Give a bounding box for every parasitised red blood cell, every trophozoite, every gametocyte, every leukocyte, and every artifact (platelet-like body, stain precipitate, or debris).
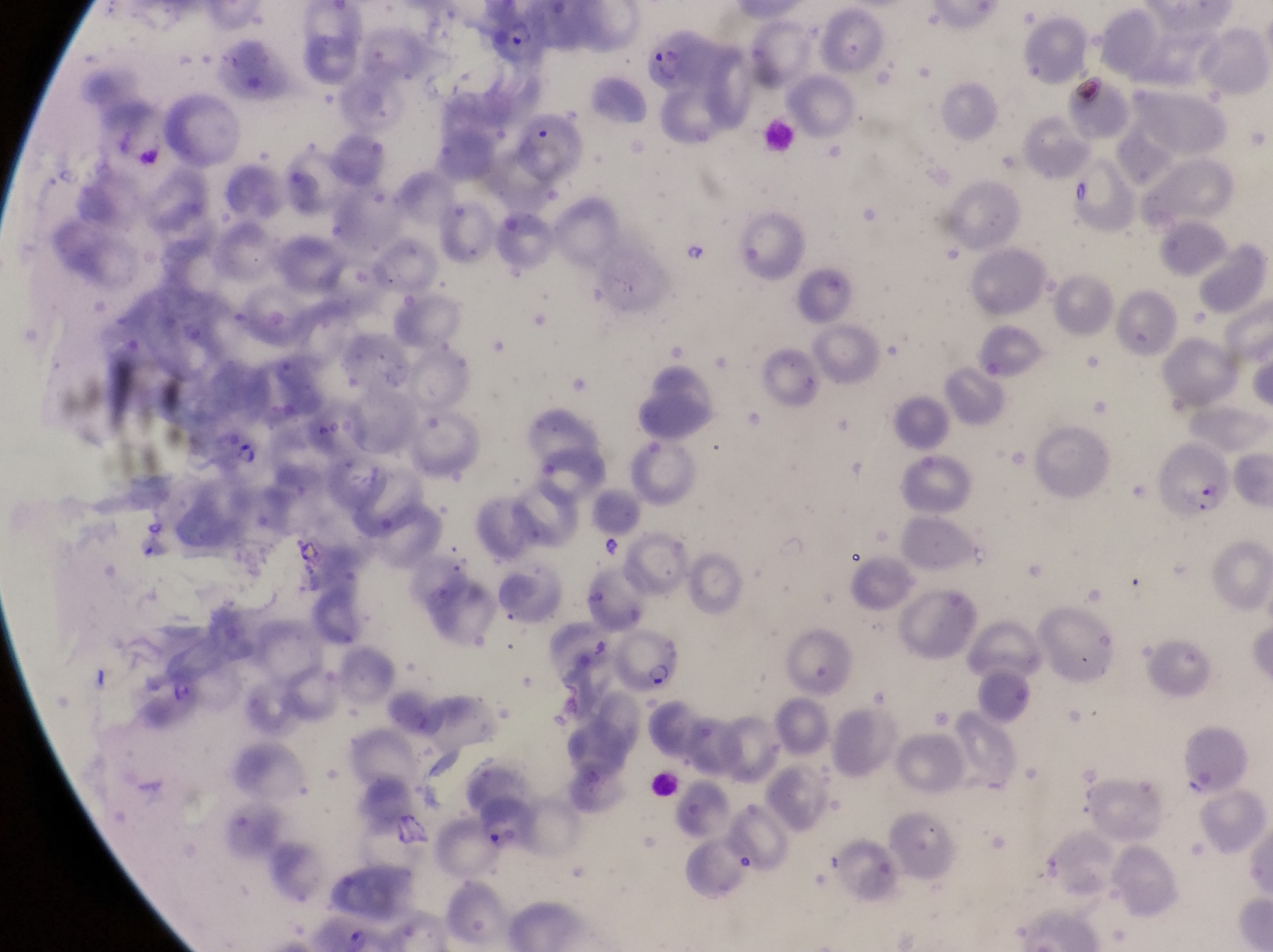
Approximate bounding boxes as {left, top, right, bottom} in pixels.
Parasitised red blood cells: {495, 10, 557, 73}, {631, 33, 716, 91}, {1168, 430, 1240, 523}, {621, 627, 688, 697}.
Trophozoites: {210, 422, 268, 477}, {292, 537, 324, 569}.
No leukocytes observed.
Artifacts (platelet-like body, stain precipitate, or debris): {1075, 70, 1109, 115}, {682, 242, 710, 269}.

{
  "capture": "smartphone photograph through the eyepiece of an Olympus CX-23 microscope",
  "image_size": "1273×952 pixels",
  "preparation": "thin blood film",
  "country": "Uganda",
  "magnification": "1000x",
  "field_of_view": "single"
}